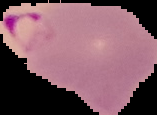

image size = 157×115 pixels
preparation = thin blood smear
image type = cell region segmented out of the field of view; surrounding area masked to black
result = Plasmodium parasites detected